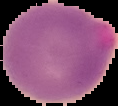
Summary:
  - Preparation: thin blood film
  - Image type: cell region segmented out of the field of view; surrounding area masked to black
  - Result: malaria parasites detected
  - Image size: 118×106 pixels